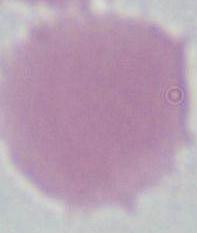 Micrograph. An erythrocyte is shown. 1000x magnification.